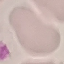
Malaria status: uninfected. Photographed with a smartphone camera at the microscope eyepiece. Thin blood smear. Giemsa stain. Automatically extracted cell patch, resized to 64 × 64 pixels.